Report the malaria status of this cell.
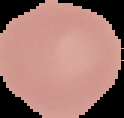
It is uninfected.

Summary:
  - Image size: 124×118 pixels
  - Image type: segmented cell region with the area outside set to black
  - Preparation: thin blood smear